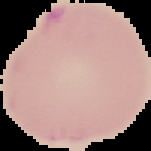
Result: Plasmodium parasites identified. Image is 151×151 pixels. From a thin blood film. Cell region segmented out of the field of view; the surrounding area is masked to black.